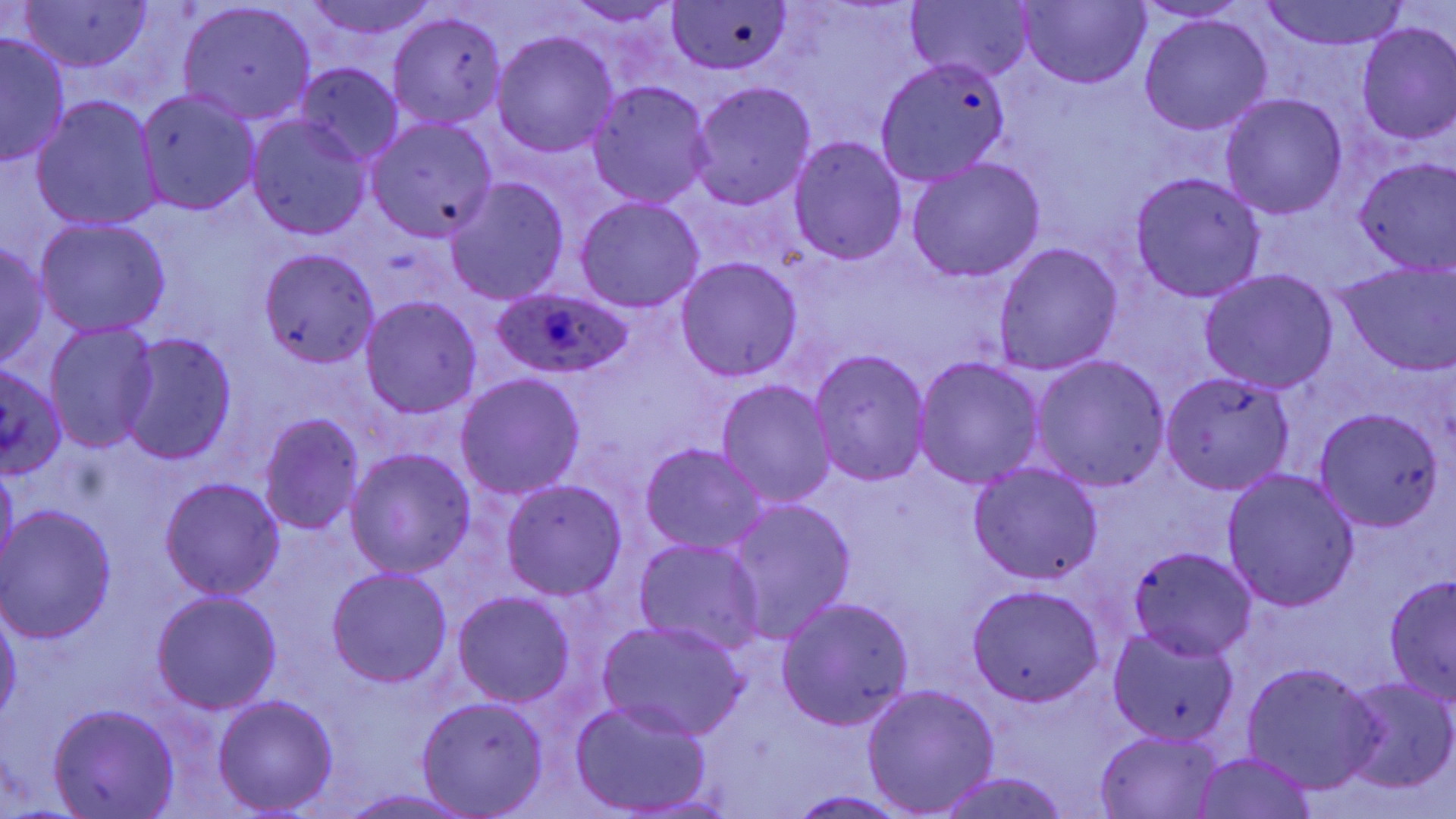
Approximate bounding boxes as named x1/y1/x2/y2 corners in pixels. Plasmodium ovale-infected red blood cell locations: (x1=489, y1=287, x2=634, y2=380). Uninfected red blood cell locations: (x1=297, y1=0, x2=438, y2=38), (x1=1259, y1=0, x2=1414, y2=51), (x1=11, y1=1, x2=155, y2=72), (x1=563, y1=1, x2=682, y2=25), (x1=905, y1=1, x2=1033, y2=82), (x1=1131, y1=1, x2=1250, y2=24), (x1=668, y1=2, x2=792, y2=75), (x1=1016, y1=2, x2=1150, y2=89), (x1=176, y1=3, x2=317, y2=126), (x1=387, y1=14, x2=507, y2=130), (x1=1139, y1=14, x2=1272, y2=136), (x1=1355, y1=21, x2=1456, y2=145), (x1=0, y1=31, x2=71, y2=167), (x1=492, y1=31, x2=619, y2=158), (x1=875, y1=59, x2=1011, y2=185), (x1=295, y1=64, x2=405, y2=167), (x1=588, y1=81, x2=716, y2=208), (x1=688, y1=81, x2=817, y2=209), (x1=136, y1=90, x2=262, y2=214), (x1=1220, y1=93, x2=1347, y2=219), (x1=30, y1=95, x2=163, y2=231), (x1=245, y1=117, x2=372, y2=240), (x1=364, y1=117, x2=499, y2=243), (x1=789, y1=137, x2=907, y2=264), (x1=1352, y1=157, x2=1456, y2=274), (x1=905, y1=158, x2=1045, y2=283), (x1=1131, y1=172, x2=1266, y2=302), (x1=445, y1=177, x2=569, y2=305), (x1=574, y1=196, x2=705, y2=313), (x1=34, y1=216, x2=172, y2=336), (x1=0, y1=240, x2=49, y2=367), (x1=994, y1=243, x2=1122, y2=376), (x1=256, y1=249, x2=379, y2=369), (x1=675, y1=257, x2=803, y2=381), (x1=1338, y1=261, x2=1456, y2=376), (x1=1199, y1=268, x2=1338, y2=393), (x1=361, y1=296, x2=482, y2=418), (x1=43, y1=320, x2=159, y2=452), (x1=119, y1=333, x2=238, y2=464), (x1=808, y1=350, x2=930, y2=486), (x1=1029, y1=355, x2=1169, y2=490), (x1=914, y1=356, x2=1045, y2=487), (x1=0, y1=360, x2=66, y2=479), (x1=1160, y1=369, x2=1297, y2=495), (x1=455, y1=373, x2=585, y2=501), (x1=715, y1=379, x2=836, y2=507), (x1=1314, y1=409, x2=1446, y2=530), (x1=258, y1=412, x2=366, y2=535), (x1=640, y1=443, x2=769, y2=556), (x1=345, y1=447, x2=476, y2=578), (x1=1, y1=461, x2=18, y2=580), (x1=968, y1=463, x2=1105, y2=586), (x1=1221, y1=469, x2=1360, y2=613), (x1=159, y1=477, x2=284, y2=600), (x1=501, y1=479, x2=627, y2=601), (x1=725, y1=497, x2=856, y2=643), (x1=1, y1=505, x2=118, y2=644), (x1=632, y1=538, x2=767, y2=657), (x1=1128, y1=547, x2=1258, y2=661), (x1=327, y1=567, x2=454, y2=687), (x1=1384, y1=572, x2=1456, y2=705), (x1=966, y1=584, x2=1105, y2=707), (x1=152, y1=590, x2=281, y2=714), (x1=453, y1=592, x2=574, y2=708), (x1=775, y1=597, x2=914, y2=732), (x1=0, y1=607, x2=21, y2=729), (x1=597, y1=621, x2=750, y2=742), (x1=1105, y1=627, x2=1240, y2=748), (x1=1244, y1=662, x2=1381, y2=792), (x1=1337, y1=676, x2=1456, y2=794), (x1=862, y1=683, x2=1000, y2=816), (x1=214, y1=694, x2=339, y2=815), (x1=416, y1=698, x2=549, y2=817), (x1=569, y1=699, x2=715, y2=815), (x1=49, y1=704, x2=180, y2=818), (x1=1095, y1=731, x2=1223, y2=818), (x1=1191, y1=755, x2=1317, y2=817), (x1=931, y1=772, x2=1074, y2=819), (x1=332, y1=789, x2=483, y2=819), (x1=784, y1=791, x2=915, y2=819). Slide-level diagnosis: Plasmodium ovale. 1000x magnification. Image is 1456×819 pixels. Light microscopy. May-Grünwald-Giemsa-stained preparation. Thin blood film. Single field of view.